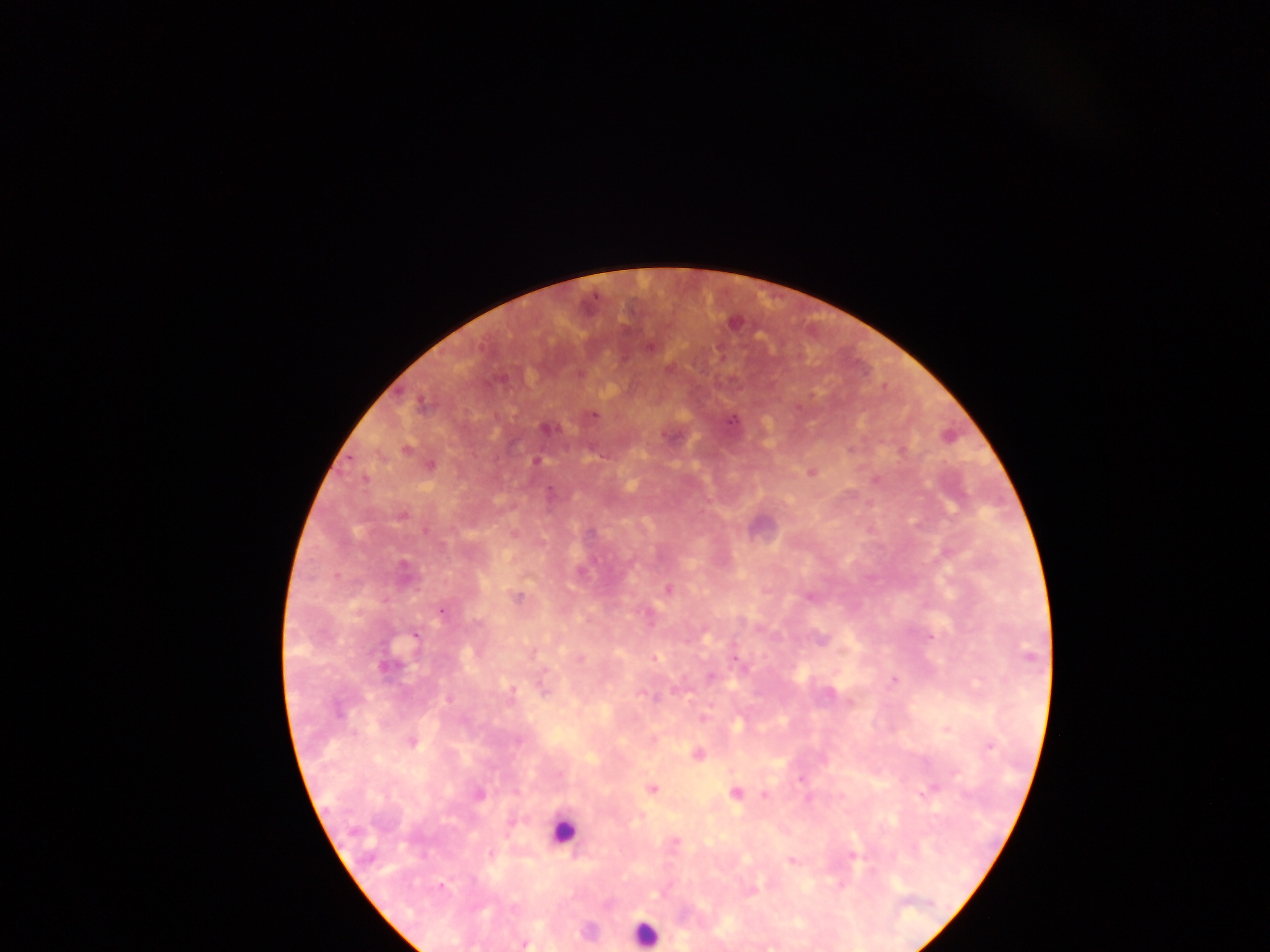

Approximate centers as (x, y) in pixels.
Summary:
  - Leukocyte locations: (565, 833), (644, 933)
  - Plasmodium parasite locations: (594, 296), (592, 414), (536, 461), (441, 611), (929, 636), (735, 657), (893, 679), (989, 747), (917, 793), (851, 855), (790, 860), (525, 943)
  - Preparation: thick blood smear
  - Capture: mobile-phone photograph through a microscope
  - Image size: 1270×952 pixels
  - Field of view: single
  - Country: Ghana